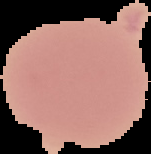 From a thin blood smear. Cell region segmented out of the field of view; the surrounding area is masked to black. Image is 151×154 pixels. Result: no malaria parasites seen.